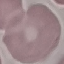
malaria status = uninfected
stain = Giemsa
image type = cell patch, automatically extracted from a larger field of view and resized to 64 × 64 pixels
capture = smartphone through the microscope eyepiece
preparation = thin blood smear